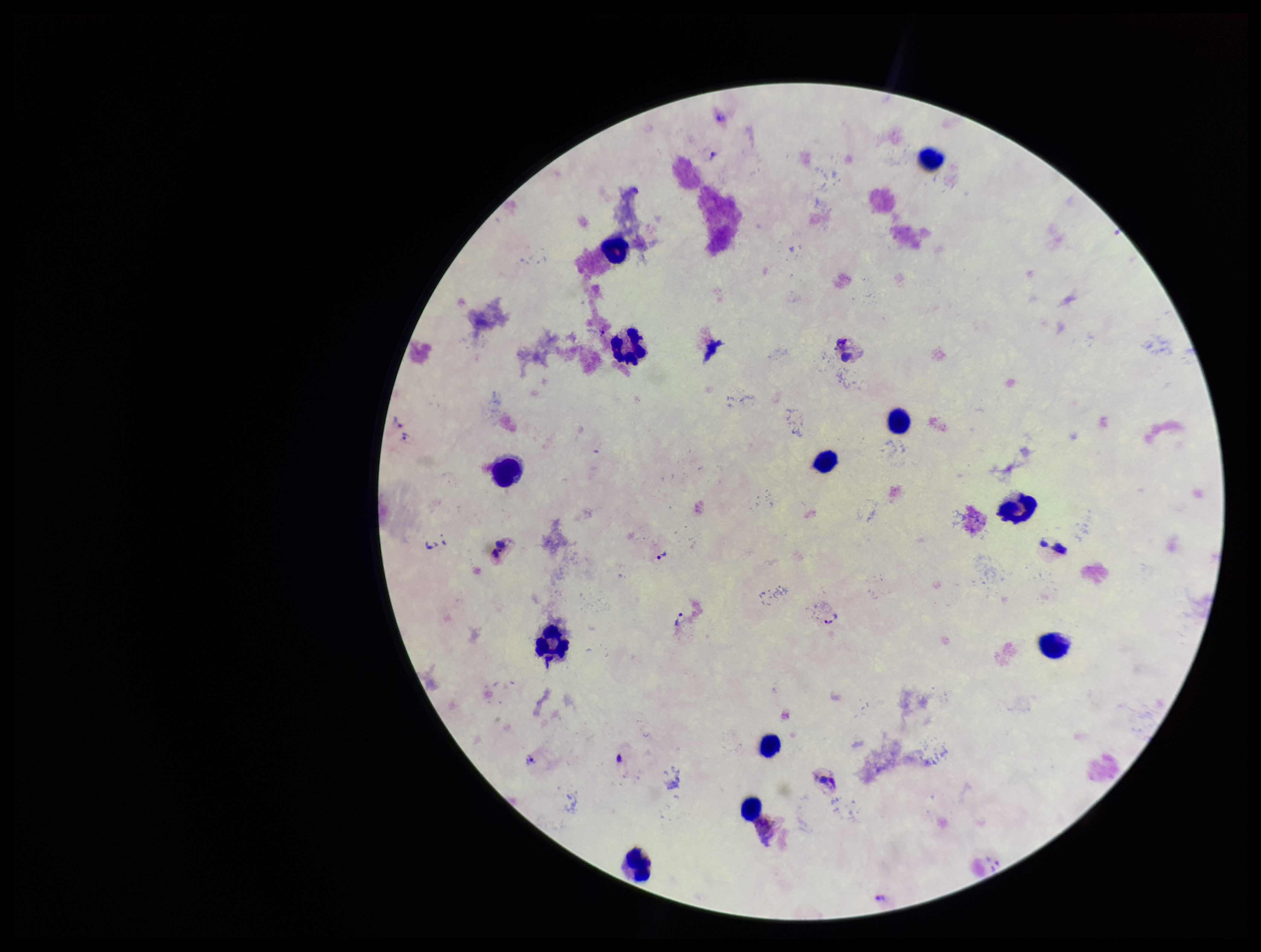

parasite count = 0
stain = Giemsa
patient malaria status = positive
capture = smartphone photograph through the microscope eyepiece
species reported for this patient = Plasmodium vivax
leukocyte count = 12
image size = 1261×952 pixels
field of view = one from this slide
preparation = thick blood smear
Plasmodium parasites = none detected